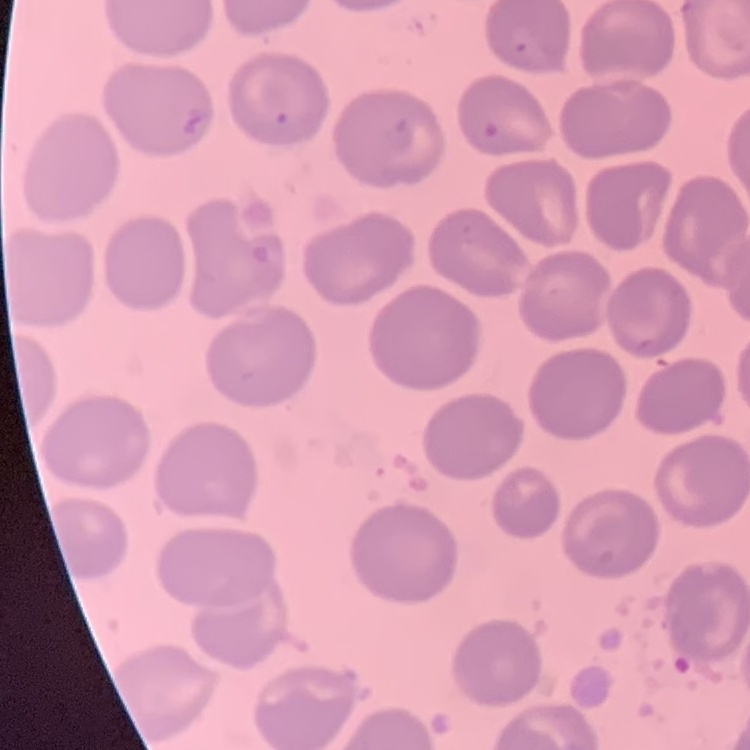 The red blood cells show no rouleaux formation. Thin blood smear. Field's or Giemsa stain. One tile cut from a larger photomicrograph.